Assess this cell for malaria.
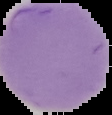
It is uninfected.

Summary:
  - Preparation: thin blood film
  - Image type: segmented cell region with the area outside set to black
  - Image size: 112×115 pixels